Locate and identify every blood parasite.
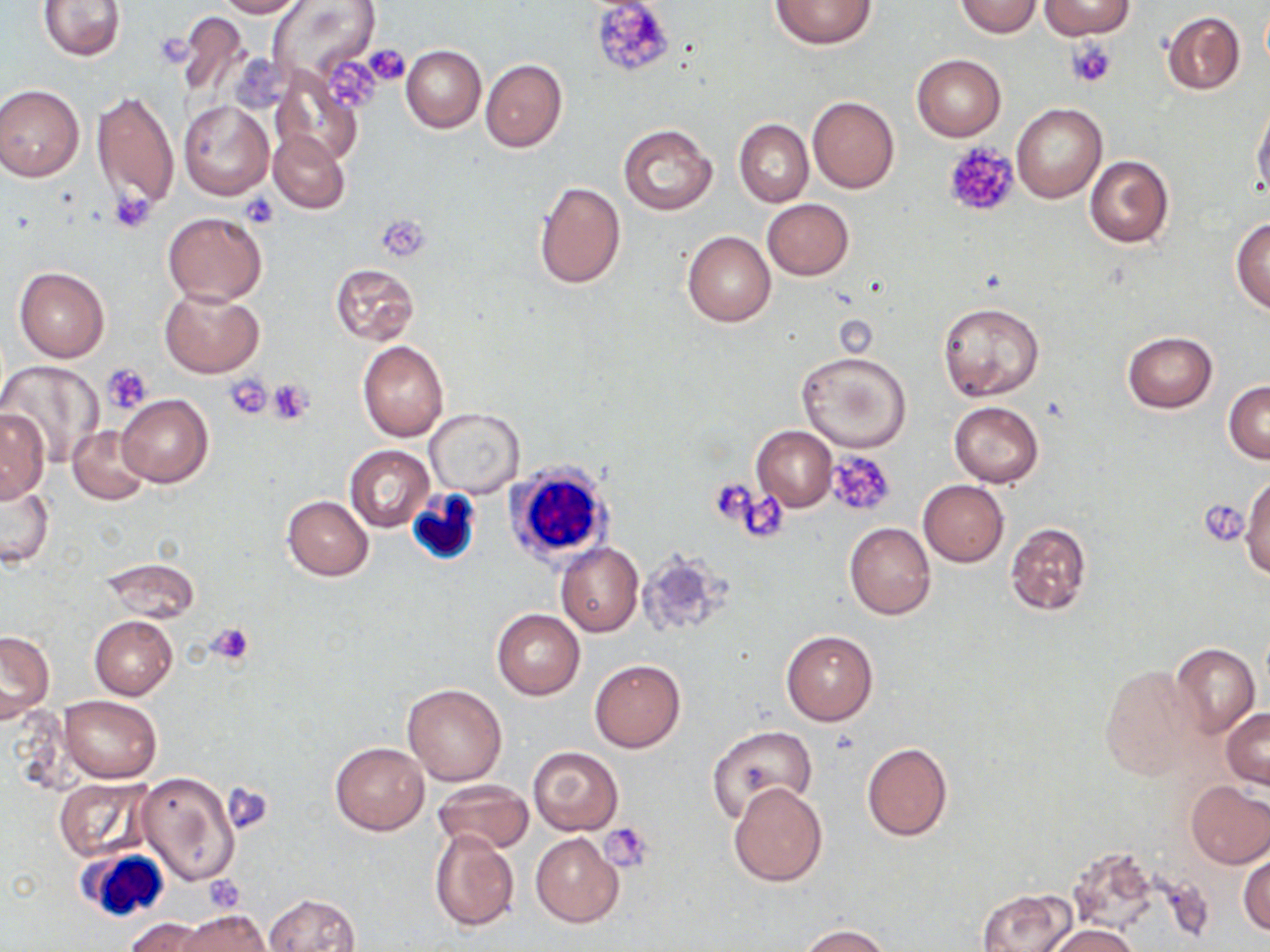

No blood parasites seen.

slide_level_diagnosis: no evidence of blood parasites
stain: May-Grünwald-Giemsa
field_of_view: one of a larger specimen
platelet_locations: 'approximate bounding boxes as named x1/y1/x2/y2 corners in pixels: (x1=590, y1=0, x2=676, y2=78), (x1=1067, y1=38, x2=1117, y2=87), (x1=361, y1=45, x2=410, y2=87), (x1=319, y1=53, x2=386, y2=114), (x1=943, y1=142, x2=1019, y2=218), (x1=109, y1=191, x2=156, y2=233), (x1=240, y1=191, x2=279, y2=228), (x1=376, y1=216, x2=429, y2=261), (x1=102, y1=362, x2=154, y2=414), (x1=223, y1=375, x2=274, y2=420), (x1=268, y1=379, x2=314, y2=424), (x1=824, y1=450, x2=897, y2=519), (x1=709, y1=478, x2=761, y2=531), (x1=734, y1=491, x2=791, y2=542), (x1=1201, y1=498, x2=1249, y2=547), (x1=206, y1=621, x2=256, y2=665), (x1=223, y1=783, x2=275, y2=834), (x1=599, y1=824, x2=653, y2=871), (x1=203, y1=876, x2=246, y2=912)'
white_blood_cell_locations: 'approximate bounding boxes as named x1/y1/x2/y2 corners in pixels: (x1=504, y1=460, x2=615, y2=571), (x1=408, y1=480, x2=480, y2=565), (x1=76, y1=848, x2=171, y2=922)'
image_size: 1270×952 pixels
uninfected_red_blood_cell_locations: 'approximate bounding boxes as named x1/y1/x2/y2 corners in pixels: (x1=214, y1=0, x2=306, y2=18), (x1=270, y1=0, x2=384, y2=88), (x1=770, y1=0, x2=875, y2=49), (x1=38, y1=1, x2=126, y2=62), (x1=955, y1=1, x2=1042, y2=37), (x1=1040, y1=1, x2=1137, y2=38), (x1=1162, y1=11, x2=1245, y2=95), (x1=172, y1=12, x2=252, y2=102), (x1=401, y1=46, x2=485, y2=132), (x1=913, y1=54, x2=1006, y2=142), (x1=480, y1=59, x2=568, y2=153), (x1=271, y1=68, x2=364, y2=166), (x1=0, y1=84, x2=84, y2=181), (x1=91, y1=89, x2=179, y2=216), (x1=808, y1=96, x2=900, y2=194), (x1=179, y1=100, x2=273, y2=198), (x1=1252, y1=103, x2=1270, y2=199), (x1=1012, y1=104, x2=1106, y2=203), (x1=734, y1=119, x2=813, y2=207), (x1=618, y1=124, x2=717, y2=217), (x1=268, y1=129, x2=350, y2=214), (x1=1084, y1=155, x2=1175, y2=249), (x1=532, y1=181, x2=625, y2=288), (x1=762, y1=199, x2=854, y2=280), (x1=163, y1=210, x2=267, y2=305), (x1=1230, y1=217, x2=1270, y2=314), (x1=683, y1=232, x2=775, y2=327), (x1=329, y1=263, x2=419, y2=344), (x1=13, y1=267, x2=109, y2=362), (x1=159, y1=289, x2=263, y2=377), (x1=939, y1=303, x2=1045, y2=402), (x1=1122, y1=331, x2=1218, y2=413), (x1=357, y1=339, x2=449, y2=441), (x1=795, y1=351, x2=912, y2=453), (x1=2, y1=361, x2=104, y2=465), (x1=1224, y1=380, x2=1270, y2=463), (x1=117, y1=395, x2=213, y2=487), (x1=949, y1=401, x2=1044, y2=486), (x1=425, y1=408, x2=524, y2=498), (x1=1, y1=409, x2=49, y2=500), (x1=68, y1=425, x2=153, y2=504), (x1=752, y1=426, x2=837, y2=511), (x1=345, y1=444, x2=434, y2=531), (x1=1, y1=473, x2=55, y2=570), (x1=1241, y1=474, x2=1269, y2=579), (x1=918, y1=480, x2=1008, y2=567), (x1=281, y1=495, x2=374, y2=580), (x1=1005, y1=521, x2=1093, y2=616), (x1=844, y1=523, x2=936, y2=619), (x1=556, y1=542, x2=644, y2=637), (x1=636, y1=548, x2=729, y2=638), (x1=98, y1=556, x2=199, y2=624), (x1=491, y1=609, x2=584, y2=699), (x1=89, y1=615, x2=177, y2=699), (x1=0, y1=629, x2=54, y2=722), (x1=781, y1=630, x2=877, y2=725), (x1=1170, y1=643, x2=1259, y2=738), (x1=590, y1=659, x2=686, y2=753), (x1=1097, y1=664, x2=1203, y2=781), (x1=402, y1=683, x2=506, y2=786), (x1=59, y1=695, x2=162, y2=783), (x1=1222, y1=708, x2=1269, y2=788), (x1=706, y1=724, x2=818, y2=821), (x1=329, y1=742, x2=428, y2=835), (x1=862, y1=743, x2=953, y2=841), (x1=528, y1=746, x2=623, y2=834), (x1=134, y1=771, x2=241, y2=886), (x1=54, y1=775, x2=155, y2=862), (x1=432, y1=779, x2=534, y2=854), (x1=1184, y1=781, x2=1270, y2=868), (x1=727, y1=782, x2=828, y2=887), (x1=429, y1=826, x2=520, y2=932), (x1=530, y1=832, x2=624, y2=927), (x1=1071, y1=851, x2=1159, y2=937), (x1=1239, y1=853, x2=1270, y2=937), (x1=977, y1=888, x2=1076, y2=952), (x1=262, y1=893, x2=362, y2=952), (x1=173, y1=907, x2=272, y2=951), (x1=125, y1=917, x2=213, y2=952), (x1=1045, y1=923, x2=1138, y2=952), (x1=799, y1=925, x2=892, y2=952)'
preparation: thin blood smear
magnification: 1000x
modality: light microscopy